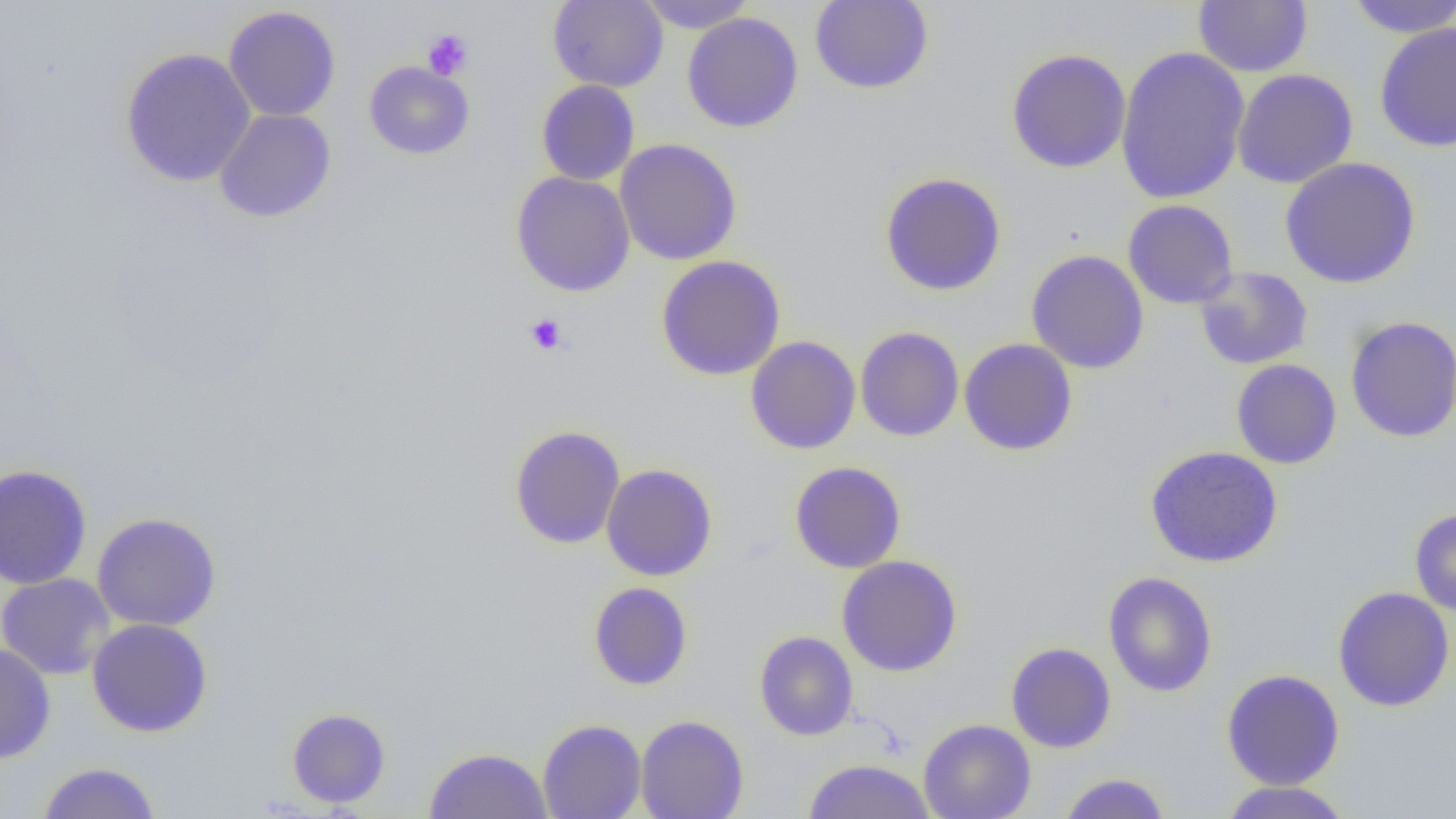
Summary:
  - Coordinate format: approximate bounding boxes as named x1/y1/x2/y2 corners in pixels
  - Platelet locations: (x1=422, y1=29, x2=474, y2=80), (x1=524, y1=313, x2=568, y2=356)
  - Uninfected red blood cell locations: (x1=547, y1=0, x2=668, y2=92), (x1=636, y1=0, x2=757, y2=32), (x1=1193, y1=0, x2=1312, y2=77), (x1=1344, y1=0, x2=1456, y2=37), (x1=810, y1=1, x2=934, y2=94), (x1=223, y1=5, x2=341, y2=122), (x1=682, y1=12, x2=804, y2=133), (x1=1375, y1=22, x2=1456, y2=152), (x1=1115, y1=45, x2=1250, y2=205), (x1=120, y1=47, x2=256, y2=187), (x1=1005, y1=49, x2=1132, y2=173), (x1=363, y1=61, x2=474, y2=160), (x1=1231, y1=68, x2=1358, y2=189), (x1=536, y1=80, x2=639, y2=185), (x1=214, y1=109, x2=336, y2=223), (x1=614, y1=138, x2=742, y2=266), (x1=1280, y1=157, x2=1421, y2=288), (x1=511, y1=171, x2=636, y2=297), (x1=879, y1=172, x2=1007, y2=296), (x1=1123, y1=199, x2=1239, y2=309), (x1=1026, y1=250, x2=1150, y2=374), (x1=656, y1=255, x2=786, y2=380), (x1=1193, y1=266, x2=1314, y2=370), (x1=1345, y1=315, x2=1456, y2=443), (x1=855, y1=326, x2=964, y2=442), (x1=745, y1=336, x2=861, y2=454), (x1=958, y1=338, x2=1078, y2=457), (x1=1231, y1=359, x2=1342, y2=469), (x1=509, y1=425, x2=626, y2=549), (x1=1144, y1=445, x2=1283, y2=568), (x1=789, y1=461, x2=906, y2=573), (x1=601, y1=463, x2=717, y2=581), (x1=0, y1=464, x2=93, y2=590), (x1=1409, y1=509, x2=1456, y2=616), (x1=92, y1=513, x2=221, y2=631), (x1=836, y1=555, x2=963, y2=676), (x1=1102, y1=571, x2=1218, y2=698), (x1=0, y1=573, x2=115, y2=680), (x1=588, y1=581, x2=693, y2=690), (x1=1332, y1=586, x2=1455, y2=712), (x1=86, y1=618, x2=213, y2=737), (x1=753, y1=631, x2=859, y2=741), (x1=1005, y1=642, x2=1116, y2=752), (x1=0, y1=643, x2=56, y2=764), (x1=1221, y1=669, x2=1345, y2=790), (x1=286, y1=708, x2=391, y2=808), (x1=636, y1=715, x2=748, y2=819), (x1=537, y1=718, x2=647, y2=819), (x1=918, y1=718, x2=1036, y2=819), (x1=424, y1=747, x2=553, y2=818), (x1=801, y1=759, x2=936, y2=819), (x1=36, y1=761, x2=162, y2=819), (x1=1057, y1=772, x2=1171, y2=819), (x1=1218, y1=780, x2=1354, y2=818)
  - Slide-level diagnosis: no evidence of blood parasites
  - Preparation: thin blood film
  - Field of view: single
  - Magnification: 1000x
  - Image size: 1456×819 pixels
  - Modality: light microscopy